Assess the morphology of the erythrocytes.
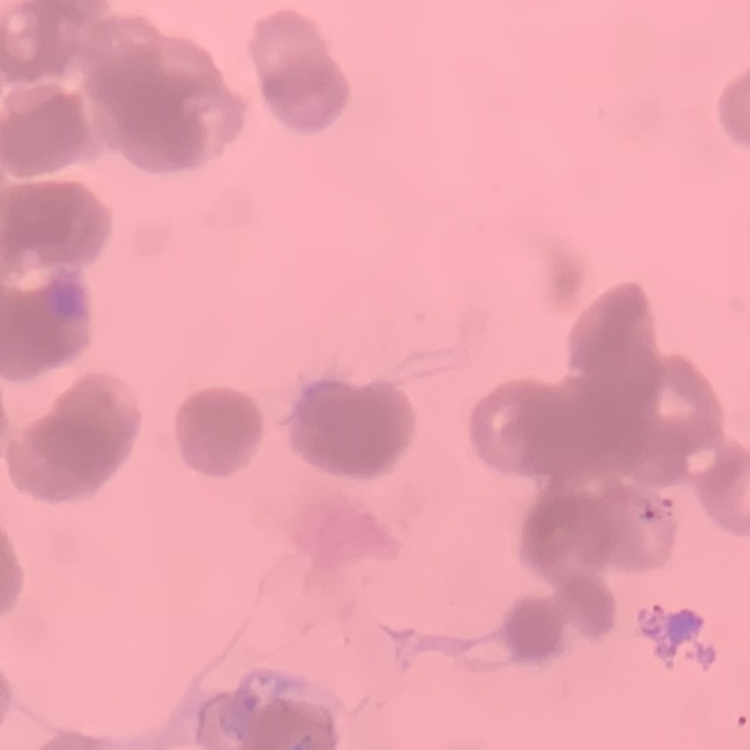
Rouleaux formation.

Summary:
  - Image type: one tile cut from a larger photomicrograph
  - Stain: Field's or Giemsa
  - Preparation: thin peripheral smear